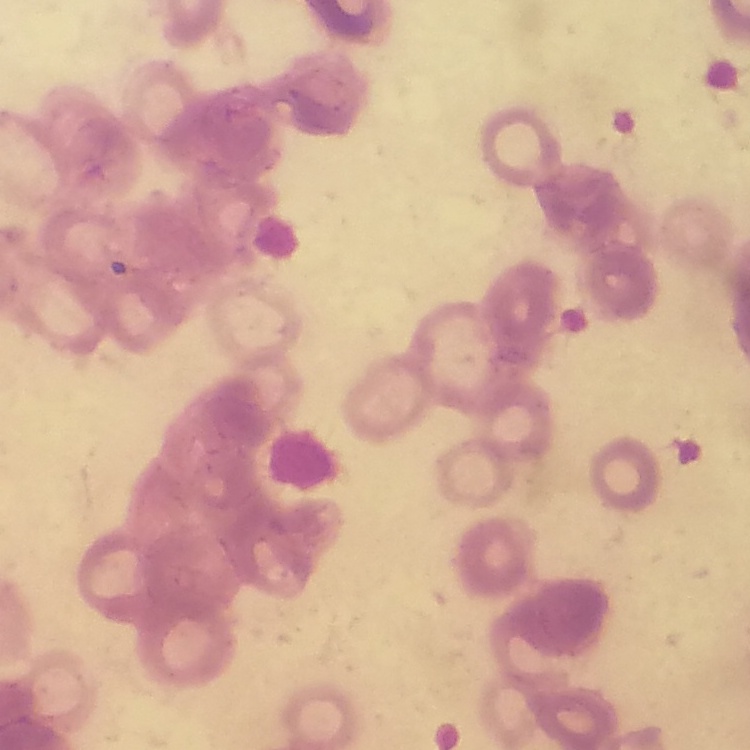
The erythrocytes exhibit rouleaux formation. One tile cut from a larger photomicrograph. Stained with either Field's or Giemsa. Thin blood smear.